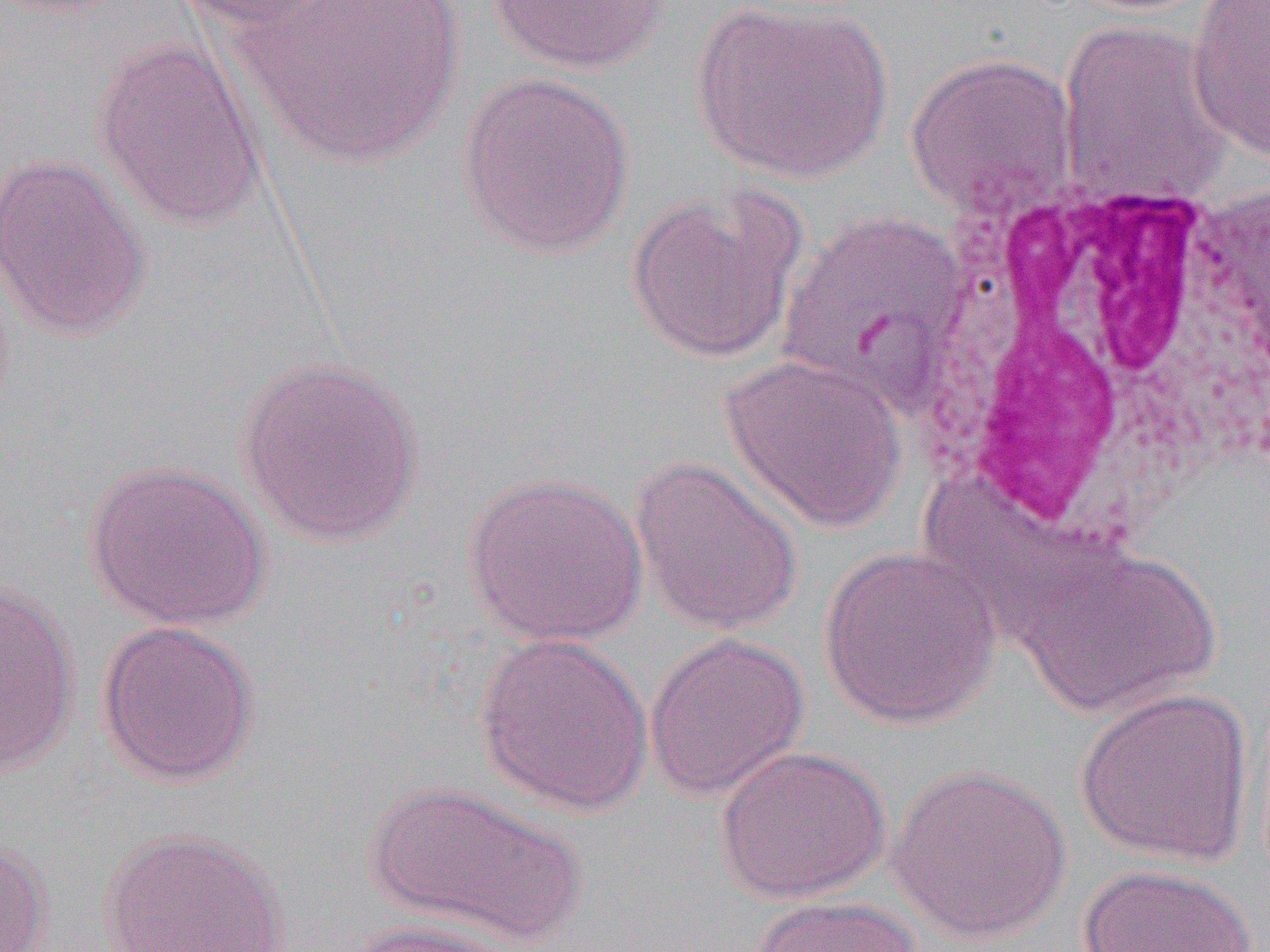

{
  "slide_level_diagnosis": "Plasmodium vivax",
  "image_size": "1270×952 pixels",
  "uninfected_red_blood_cell_locations": "approximate bounding boxes as (x1,y1)-(x2,y2) corner pairs in pixels: (172,0)-(355,32), (239,0)-(466,168), (485,0)-(676,75), (691,0)-(893,183), (1185,0)-(1270,161), (1057,19)-(1234,207), (90,37)-(267,230), (904,51)-(1080,219), (457,72)-(635,259), (0,152)-(151,341), (624,184)-(806,364), (778,211)-(968,404), (719,354)-(908,534), (235,355)-(425,547), (629,456)-(803,636), (83,459)-(272,631), (461,471)-(649,647), (1010,541)-(1222,719), (817,545)-(1001,731), (0,581)-(80,774), (96,620)-(260,787), (475,630)-(654,815), (643,633)-(809,802), (1073,687)-(1255,867), (714,744)-(891,903), (888,762)-(1071,945), (364,780)-(587,949), (98,828)-(292,951), (0,833)-(53,952), (1078,864)-(1256,952), (746,895)-(926,952), (341,918)-(523,951)",
  "magnification": "1000x",
  "modality": "light microscopy",
  "preparation": "thin blood smear",
  "field_of_view": "one of a larger specimen",
  "white_blood_cell_locations": "approximate bounding boxes as (x1,y1)-(x2,y2) corner pairs in pixels: (904,170)-(1270,530)"
}